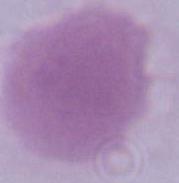

{
  "identification": "erythrocyte",
  "magnification": "1000x",
  "modality": "micrograph"
}